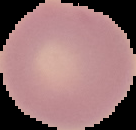
Summary:
  - Preparation: thin blood film
  - Image size: 136×130 pixels
  - Image type: segmented cell region with the area outside set to black
  - Malaria status: uninfected